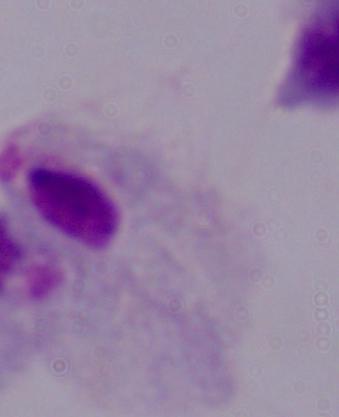 A trichomonad is shown. 1000x magnification. Micrograph.